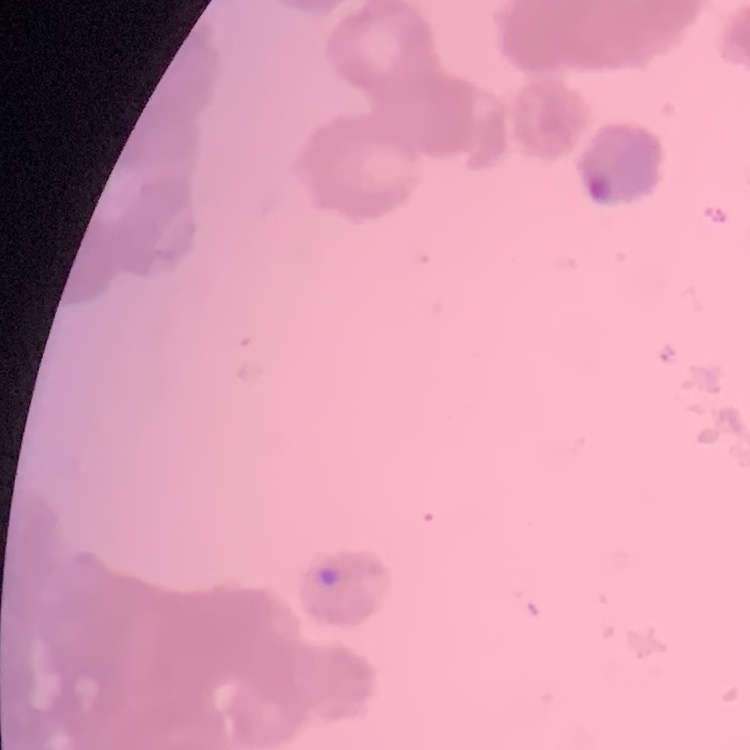
Summary:
  - Erythrocyte morphology: rouleaux formation
  - Image type: square crop of a larger photomicrograph
  - Stain: Field's or Giemsa
  - Preparation: thin peripheral smear